Locate and identify every blood parasite.
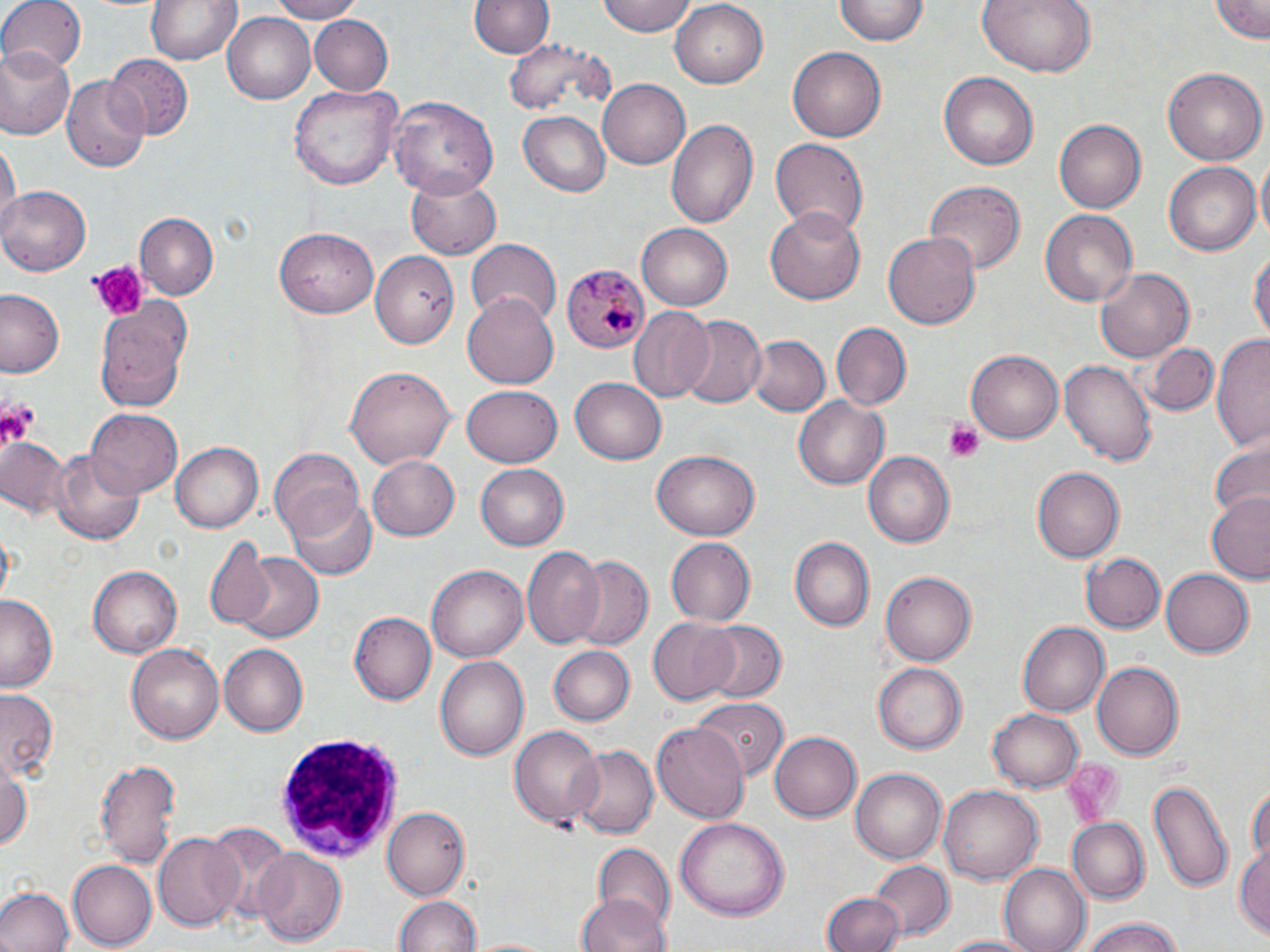
Approximate bounding boxes as named x1/y1/x2/y2 corners in pixels.
Plasmodium malariae-infected red blood cells: (x1=563, y1=264, x2=650, y2=355).
No Plasmodium falciparum, Plasmodium ovale, Plasmodium vivax, Babesia divergens, or Trypanosoma brucei observed.

Summary:
  - Uninfected red blood cell locations: (x1=0, y1=0, x2=85, y2=76), (x1=264, y1=0, x2=364, y2=23), (x1=598, y1=0, x2=697, y2=37), (x1=835, y1=0, x2=929, y2=46), (x1=977, y1=0, x2=1098, y2=77), (x1=1209, y1=0, x2=1270, y2=43), (x1=144, y1=1, x2=242, y2=66), (x1=470, y1=1, x2=552, y2=59), (x1=671, y1=1, x2=769, y2=89), (x1=223, y1=12, x2=318, y2=104), (x1=312, y1=14, x2=394, y2=94), (x1=504, y1=40, x2=611, y2=116), (x1=2, y1=48, x2=76, y2=141), (x1=788, y1=48, x2=885, y2=142), (x1=107, y1=54, x2=194, y2=140), (x1=1162, y1=66, x2=1267, y2=166), (x1=938, y1=70, x2=1039, y2=170), (x1=61, y1=76, x2=149, y2=175), (x1=596, y1=78, x2=689, y2=168), (x1=292, y1=84, x2=398, y2=192), (x1=387, y1=96, x2=499, y2=201), (x1=518, y1=111, x2=609, y2=195), (x1=666, y1=118, x2=757, y2=229), (x1=1055, y1=120, x2=1145, y2=212), (x1=2, y1=135, x2=18, y2=235), (x1=769, y1=137, x2=869, y2=238), (x1=1255, y1=156, x2=1270, y2=248), (x1=1163, y1=163, x2=1259, y2=257), (x1=404, y1=170, x2=500, y2=259), (x1=926, y1=181, x2=1024, y2=276), (x1=0, y1=184, x2=92, y2=273), (x1=766, y1=209, x2=867, y2=305), (x1=1039, y1=209, x2=1137, y2=305), (x1=135, y1=212, x2=218, y2=297), (x1=636, y1=223, x2=733, y2=310), (x1=273, y1=226, x2=378, y2=317), (x1=883, y1=230, x2=981, y2=333), (x1=466, y1=239, x2=561, y2=327), (x1=1249, y1=244, x2=1269, y2=352), (x1=373, y1=249, x2=460, y2=347), (x1=1093, y1=267, x2=1194, y2=364), (x1=93, y1=290, x2=189, y2=407), (x1=0, y1=291, x2=65, y2=378), (x1=463, y1=293, x2=559, y2=387), (x1=629, y1=309, x2=718, y2=403), (x1=677, y1=315, x2=767, y2=409), (x1=830, y1=322, x2=909, y2=410), (x1=1211, y1=333, x2=1270, y2=452), (x1=747, y1=335, x2=828, y2=418), (x1=1144, y1=340, x2=1220, y2=415), (x1=965, y1=350, x2=1064, y2=445), (x1=1059, y1=358, x2=1156, y2=465), (x1=345, y1=366, x2=455, y2=468), (x1=570, y1=375, x2=669, y2=464), (x1=460, y1=386, x2=563, y2=468), (x1=794, y1=396, x2=889, y2=489), (x1=85, y1=410, x2=182, y2=499), (x1=1, y1=435, x2=76, y2=524), (x1=170, y1=441, x2=263, y2=534), (x1=1209, y1=444, x2=1270, y2=525), (x1=268, y1=447, x2=365, y2=541), (x1=650, y1=451, x2=761, y2=539), (x1=49, y1=452, x2=143, y2=547), (x1=865, y1=452, x2=954, y2=549), (x1=365, y1=453, x2=459, y2=542), (x1=475, y1=464, x2=570, y2=551), (x1=1033, y1=465, x2=1126, y2=563), (x1=285, y1=490, x2=377, y2=579), (x1=1206, y1=493, x2=1270, y2=581), (x1=789, y1=536, x2=876, y2=632), (x1=205, y1=538, x2=277, y2=630), (x1=663, y1=538, x2=755, y2=626), (x1=521, y1=547, x2=607, y2=651), (x1=1080, y1=551, x2=1164, y2=634), (x1=233, y1=552, x2=323, y2=645), (x1=569, y1=555, x2=653, y2=650), (x1=88, y1=565, x2=181, y2=657), (x1=428, y1=565, x2=528, y2=663), (x1=1160, y1=567, x2=1254, y2=658), (x1=880, y1=571, x2=975, y2=666), (x1=1, y1=593, x2=60, y2=691), (x1=349, y1=612, x2=434, y2=706), (x1=645, y1=616, x2=741, y2=704), (x1=697, y1=620, x2=786, y2=705), (x1=1017, y1=622, x2=1108, y2=718), (x1=126, y1=642, x2=225, y2=745), (x1=218, y1=644, x2=308, y2=737), (x1=550, y1=645, x2=635, y2=727), (x1=434, y1=654, x2=530, y2=763), (x1=1090, y1=661, x2=1183, y2=761), (x1=874, y1=663, x2=969, y2=753), (x1=0, y1=687, x2=61, y2=781), (x1=691, y1=698, x2=787, y2=781), (x1=991, y1=707, x2=1084, y2=790), (x1=653, y1=720, x2=749, y2=826), (x1=508, y1=727, x2=603, y2=830), (x1=770, y1=729, x2=862, y2=820), (x1=567, y1=744, x2=657, y2=841), (x1=95, y1=756, x2=181, y2=872), (x1=0, y1=761, x2=33, y2=850), (x1=850, y1=767, x2=947, y2=865), (x1=1149, y1=776, x2=1232, y2=893), (x1=1247, y1=781, x2=1268, y2=871), (x1=940, y1=784, x2=1042, y2=886), (x1=381, y1=807, x2=467, y2=899), (x1=676, y1=816, x2=790, y2=920), (x1=1067, y1=818, x2=1150, y2=901), (x1=204, y1=821, x2=289, y2=918), (x1=152, y1=833, x2=245, y2=932), (x1=592, y1=841, x2=674, y2=930), (x1=1235, y1=843, x2=1269, y2=941), (x1=252, y1=848, x2=346, y2=944), (x1=871, y1=860, x2=953, y2=943), (x1=67, y1=862, x2=157, y2=947), (x1=999, y1=865, x2=1089, y2=952), (x1=0, y1=887, x2=72, y2=952), (x1=822, y1=892, x2=904, y2=952), (x1=574, y1=893, x2=671, y2=952), (x1=392, y1=895, x2=480, y2=952), (x1=1073, y1=918, x2=1190, y2=952), (x1=935, y1=933, x2=1048, y2=952), (x1=469, y1=935, x2=551, y2=952)
  - Platelet locations: (x1=87, y1=262, x2=149, y2=324), (x1=0, y1=396, x2=39, y2=449), (x1=944, y1=419, x2=987, y2=460), (x1=1067, y1=755, x2=1120, y2=824)
  - White blood cell locations: (x1=272, y1=736, x2=409, y2=861)
  - Slide-level diagnosis: Plasmodium malariae
  - Image size: 1270×952 pixels
  - Magnification: 1000x
  - Preparation: thin blood film
  - Field of view: one of a larger specimen
  - Modality: optical microscopy
  - Stain: May-Grünwald-Giemsa